State which parasite is depicted.
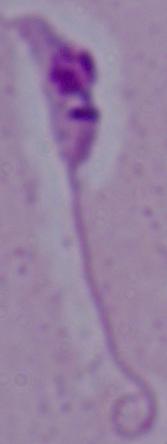

Leishmania.

magnification = 1000x
modality = photomicrograph